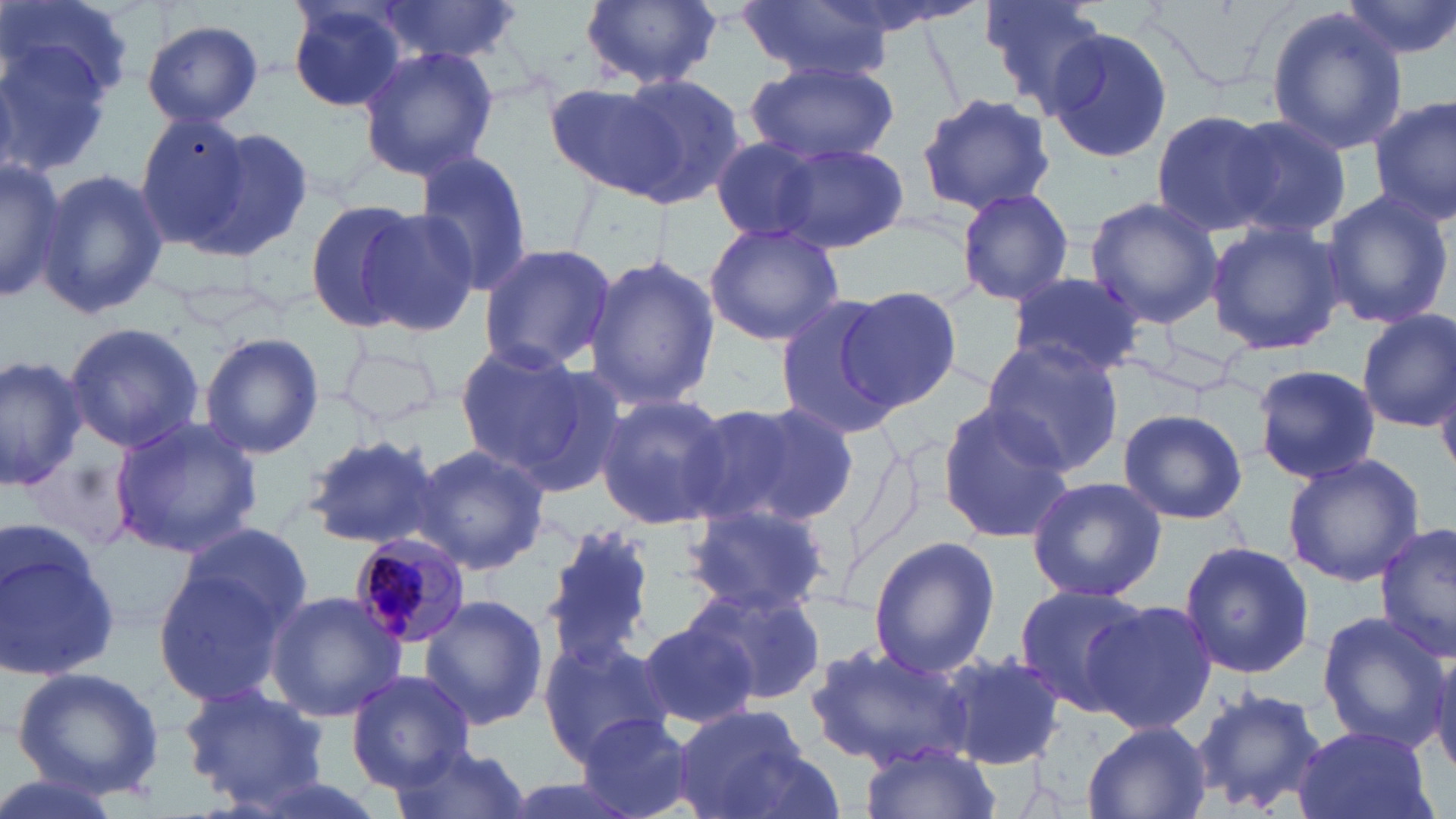
Summary:
  - Coordinate format: approximate bounding boxes as named x1/y1/x2/y2 corners in pixels
  - Uninfected red blood cell locations: (x1=579, y1=0, x2=724, y2=91), (x1=981, y1=0, x2=1108, y2=108), (x1=1339, y1=0, x2=1456, y2=64), (x1=1, y1=1, x2=134, y2=105), (x1=372, y1=1, x2=521, y2=61), (x1=285, y1=2, x2=411, y2=115), (x1=739, y1=3, x2=893, y2=82), (x1=1266, y1=8, x2=1405, y2=156), (x1=142, y1=19, x2=264, y2=127), (x1=0, y1=24, x2=123, y2=182), (x1=1042, y1=26, x2=1173, y2=166), (x1=357, y1=46, x2=500, y2=179), (x1=745, y1=61, x2=899, y2=167), (x1=597, y1=72, x2=747, y2=209), (x1=913, y1=92, x2=1055, y2=216), (x1=1370, y1=97, x2=1455, y2=227), (x1=1150, y1=110, x2=1281, y2=238), (x1=137, y1=114, x2=252, y2=248), (x1=1221, y1=115, x2=1352, y2=242), (x1=197, y1=127, x2=316, y2=262), (x1=707, y1=133, x2=843, y2=243), (x1=747, y1=136, x2=910, y2=251), (x1=410, y1=150, x2=534, y2=297), (x1=0, y1=161, x2=64, y2=305), (x1=35, y1=167, x2=169, y2=318), (x1=954, y1=186, x2=1075, y2=309), (x1=1318, y1=188, x2=1455, y2=328), (x1=1084, y1=196, x2=1223, y2=328), (x1=304, y1=198, x2=416, y2=331), (x1=356, y1=208, x2=479, y2=335), (x1=1204, y1=218, x2=1351, y2=356), (x1=703, y1=222, x2=846, y2=347), (x1=476, y1=242, x2=618, y2=373), (x1=585, y1=256, x2=720, y2=411), (x1=1006, y1=271, x2=1145, y2=379), (x1=834, y1=286, x2=962, y2=414), (x1=772, y1=294, x2=909, y2=438), (x1=1356, y1=310, x2=1456, y2=431), (x1=64, y1=320, x2=205, y2=455), (x1=199, y1=333, x2=325, y2=460), (x1=338, y1=333, x2=444, y2=431), (x1=978, y1=337, x2=1125, y2=471), (x1=453, y1=340, x2=598, y2=480), (x1=0, y1=353, x2=90, y2=489), (x1=1252, y1=363, x2=1382, y2=485), (x1=1437, y1=372, x2=1456, y2=482), (x1=594, y1=394, x2=734, y2=531), (x1=688, y1=399, x2=858, y2=532), (x1=936, y1=401, x2=1076, y2=542), (x1=1118, y1=408, x2=1248, y2=525), (x1=110, y1=416, x2=263, y2=558), (x1=302, y1=433, x2=446, y2=553), (x1=411, y1=443, x2=551, y2=574), (x1=25, y1=451, x2=136, y2=561), (x1=1283, y1=453, x2=1426, y2=586), (x1=1025, y1=476, x2=1167, y2=604), (x1=683, y1=505, x2=827, y2=617), (x1=175, y1=519, x2=313, y2=641), (x1=546, y1=523, x2=660, y2=664), (x1=1375, y1=523, x2=1456, y2=662), (x1=0, y1=526, x2=120, y2=684), (x1=867, y1=534, x2=1000, y2=679), (x1=1177, y1=540, x2=1315, y2=682), (x1=151, y1=562, x2=299, y2=708), (x1=685, y1=583, x2=825, y2=707), (x1=1010, y1=584, x2=1150, y2=715), (x1=266, y1=591, x2=407, y2=720), (x1=418, y1=596, x2=550, y2=729), (x1=1083, y1=598, x2=1216, y2=734), (x1=1315, y1=609, x2=1451, y2=751), (x1=634, y1=616, x2=760, y2=730), (x1=537, y1=632, x2=672, y2=764), (x1=804, y1=642, x2=978, y2=771), (x1=939, y1=653, x2=1067, y2=769), (x1=12, y1=666, x2=166, y2=798), (x1=345, y1=669, x2=475, y2=788), (x1=176, y1=682, x2=332, y2=811), (x1=1190, y1=685, x2=1328, y2=817), (x1=672, y1=707, x2=817, y2=819), (x1=573, y1=714, x2=698, y2=818), (x1=1082, y1=719, x2=1211, y2=819), (x1=1291, y1=724, x2=1436, y2=819), (x1=387, y1=740, x2=535, y2=819), (x1=861, y1=744, x2=999, y2=819), (x1=0, y1=770, x2=125, y2=819)
  - Plasmodium malariae-infected red blood cell locations: (x1=349, y1=533, x2=476, y2=650)
  - Slide-level diagnosis: Plasmodium malariae
  - Stain: May-Grünwald-Giemsa
  - Modality: optical microscopy
  - Image size: 1456×819 pixels
  - Field of view: one of a larger specimen
  - Magnification: 1000x
  - Preparation: thin blood smear